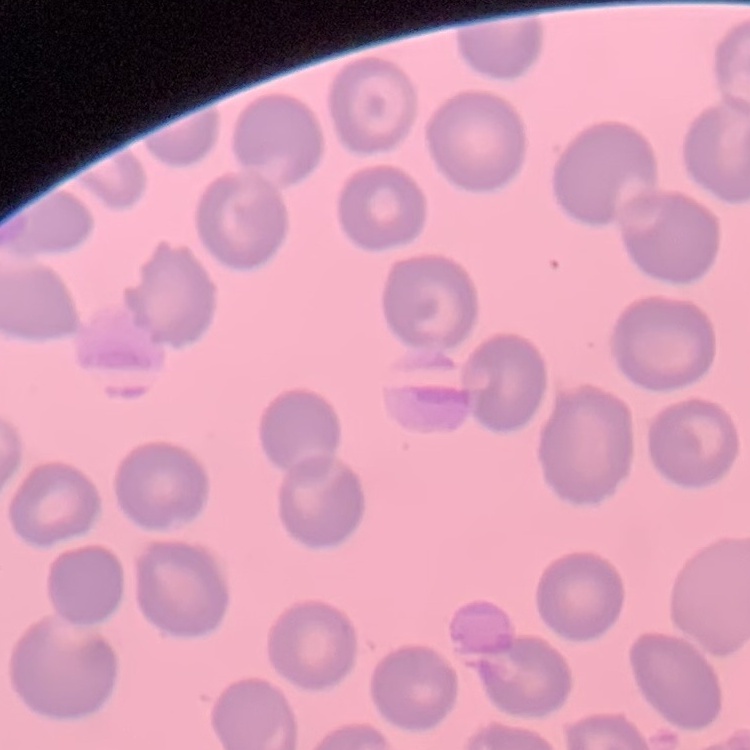
The erythrocytes show no rouleaux formation. Field's or Giemsa stain. Thin blood film. One tile cut from a larger photomicrograph.